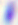

Summary:
  - Magnification: 400x
  - Identification: Toxoplasma gondii
  - Modality: photomicrograph